Comment on the morphology of the erythrocytes.
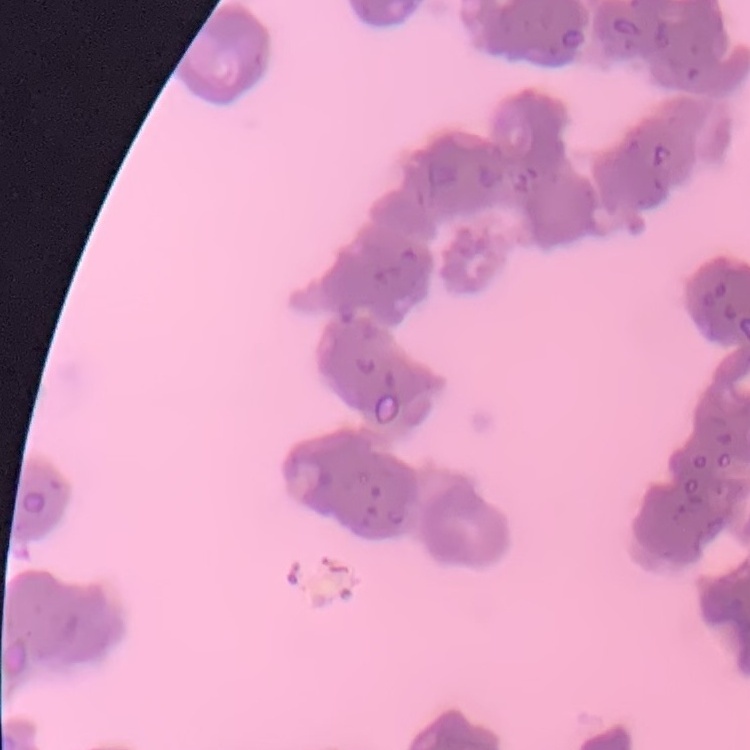

They show rouleaux formation.

preparation = thin peripheral smear
stain = Field's or Giemsa
image type = square crop of a larger photomicrograph